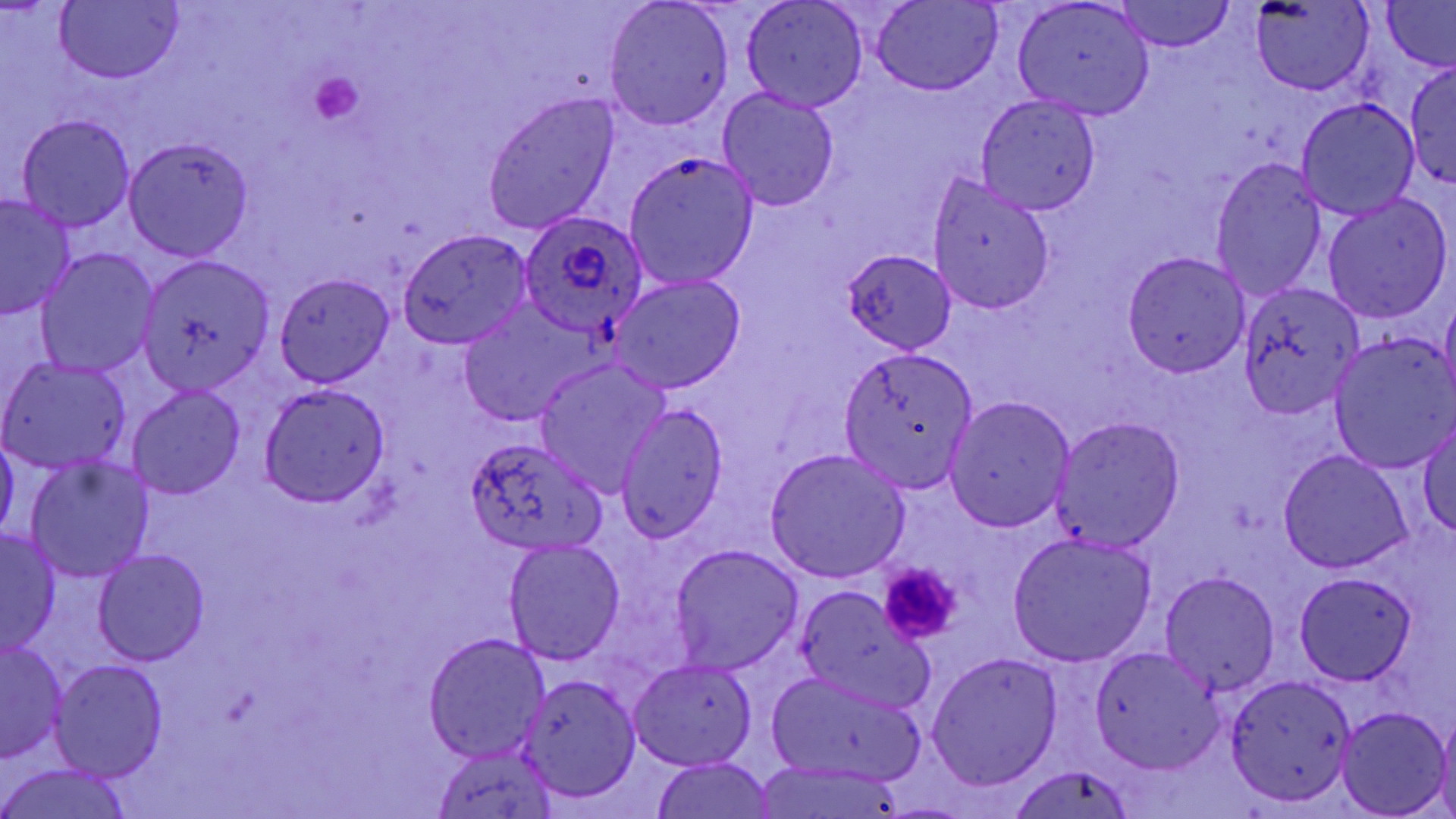
slide-level diagnosis = Plasmodium ovale
modality = light microscopy
uninfected red blood cell locations = approximate bounding boxes as (x1, y1, x2, y2) in pixels: (54, 0, 185, 84), (1115, 0, 1235, 53), (1381, 0, 1455, 72), (741, 1, 868, 112), (1251, 1, 1372, 94), (604, 2, 733, 131), (871, 2, 1001, 95), (1013, 2, 1154, 120), (1407, 63, 1456, 190), (718, 87, 840, 212), (482, 94, 618, 235), (975, 94, 1102, 215), (1297, 99, 1418, 220), (15, 115, 136, 232), (124, 138, 250, 260), (624, 150, 758, 288), (1210, 159, 1327, 302), (928, 175, 1055, 315), (1321, 193, 1452, 324), (0, 195, 75, 320), (399, 228, 536, 349), (35, 248, 158, 378), (843, 250, 957, 354), (1124, 251, 1250, 379), (138, 256, 274, 395), (275, 274, 396, 388), (606, 275, 746, 395), (1239, 286, 1366, 416), (1439, 291, 1456, 407), (454, 306, 592, 428), (1328, 336, 1456, 473), (837, 352, 978, 492), (0, 357, 133, 473), (535, 359, 669, 495), (259, 383, 390, 506), (128, 384, 245, 501), (944, 397, 1076, 531), (616, 403, 727, 543), (1051, 416, 1186, 553), (1417, 419, 1456, 538), (0, 435, 18, 544), (464, 438, 604, 553), (765, 448, 911, 582), (1279, 450, 1413, 573), (24, 455, 154, 582), (0, 528, 62, 655), (1007, 532, 1157, 667), (503, 538, 627, 664), (668, 544, 803, 676), (92, 549, 210, 667), (1159, 570, 1281, 698), (1294, 573, 1417, 686), (794, 586, 931, 710), (423, 632, 551, 762), (0, 639, 68, 763), (1090, 646, 1225, 773), (926, 653, 1063, 791), (49, 660, 169, 780), (629, 660, 757, 769), (767, 669, 926, 783), (1225, 673, 1358, 807), (517, 674, 641, 803), (1337, 706, 1450, 818), (1436, 711, 1456, 819), (432, 745, 562, 819), (648, 757, 779, 819), (0, 762, 136, 819), (1006, 764, 1136, 819), (750, 765, 909, 819)
preparation = thin blood smear
field of view = single
image size = 1456×819 pixels
Plasmodium ovale-infected red blood cell locations = approximate bounding boxes as (x1, y1, x2, y2) in pixels: (519, 209, 647, 338)
platelet locations = approximate bounding boxes as (x1, y1, x2, y2) in pixels: (309, 69, 365, 124), (877, 563, 964, 645)
stain = May-Grünwald-Giemsa
magnification = 1000x